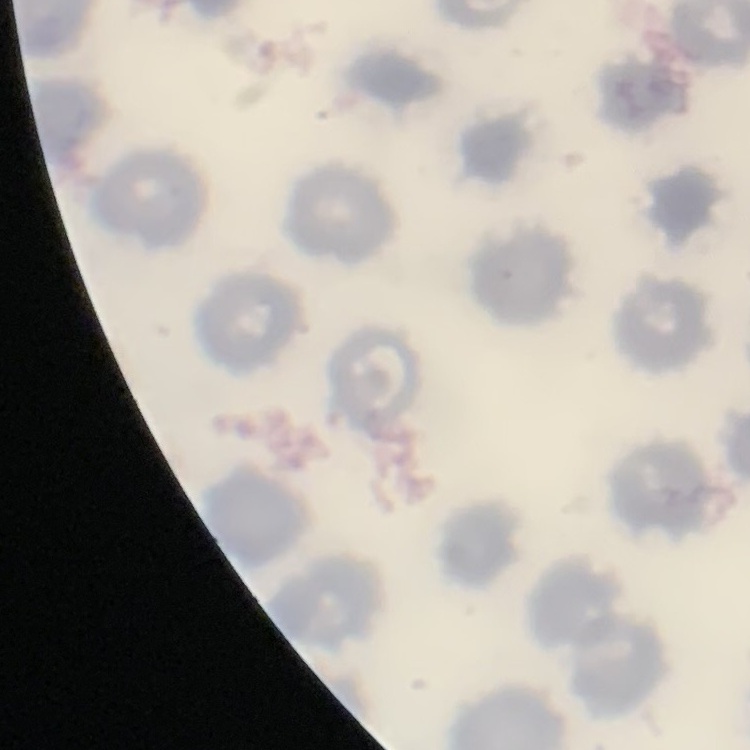

{
  "red_blood_cell_morphology": "no rouleaux formation",
  "preparation": "thin blood smear",
  "stain": "Field's or Giemsa",
  "image_type": "square crop of a larger photomicrograph"
}